Classify this cell by malaria status.
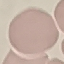

Uninfected.

Automatically extracted cell patch, resized to 64 × 64 pixels. Thin blood film. Photographed with a smartphone camera at the microscope eyepiece. Giemsa-stained preparation.